Locate every malaria parasite.
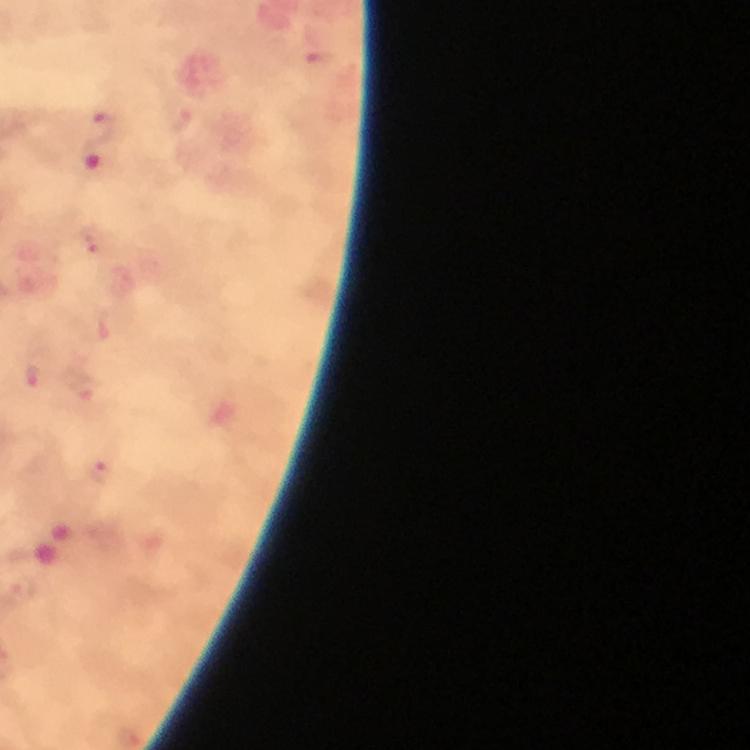
Approximate centers as [x, y] in pixels.
Malaria parasites: [105, 125], [94, 160], [94, 236], [39, 374], [96, 471].

{
  "preparation": "thick blood smear",
  "immersion_oil": "applied",
  "cropped_from": "a single field of view",
  "context": "from a malaria diagnostic workup",
  "magnification": "100x",
  "capture": "smartphone camera through the microscope",
  "stain": "Giemsa",
  "image_size": "750×750 pixels"
}